Identify the parasite.
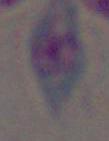
This is Toxoplasma gondii.

modality = micrograph
magnification = 1000x